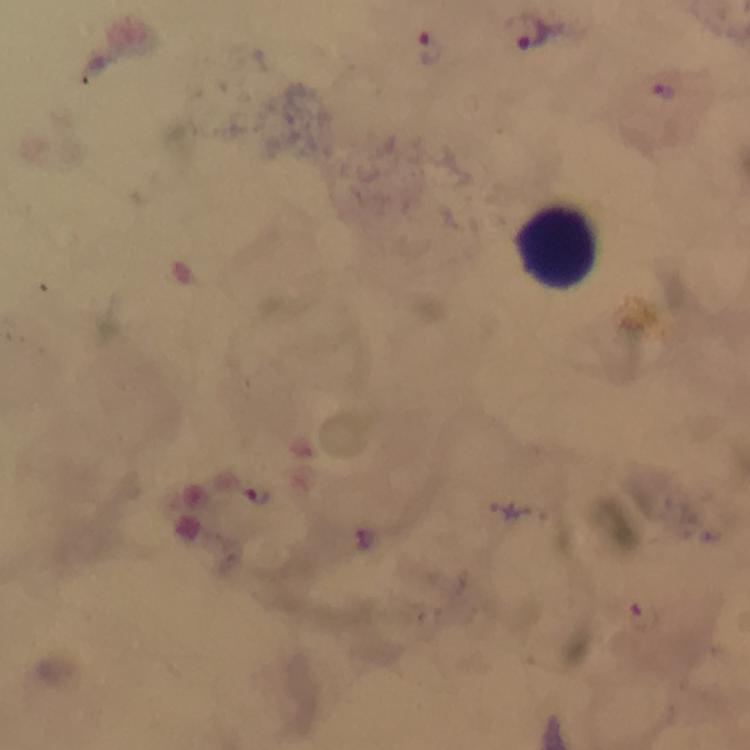
Approximate centers as [x, y] in pixels.
Summary:
  - Malaria parasite locations: [532, 34], [433, 49], [664, 91], [257, 495]
  - Leukocyte locations: [555, 247]
  - Stain: Giemsa
  - Context: from a malaria diagnostic workup
  - Magnification: 100x
  - Immersion oil: used
  - Image size: 750×750 pixels
  - Cropped from: a single field of view
  - Preparation: thick blood film
  - Capture: smartphone photograph through a microscope